Comment on the morphology of the red blood cells.
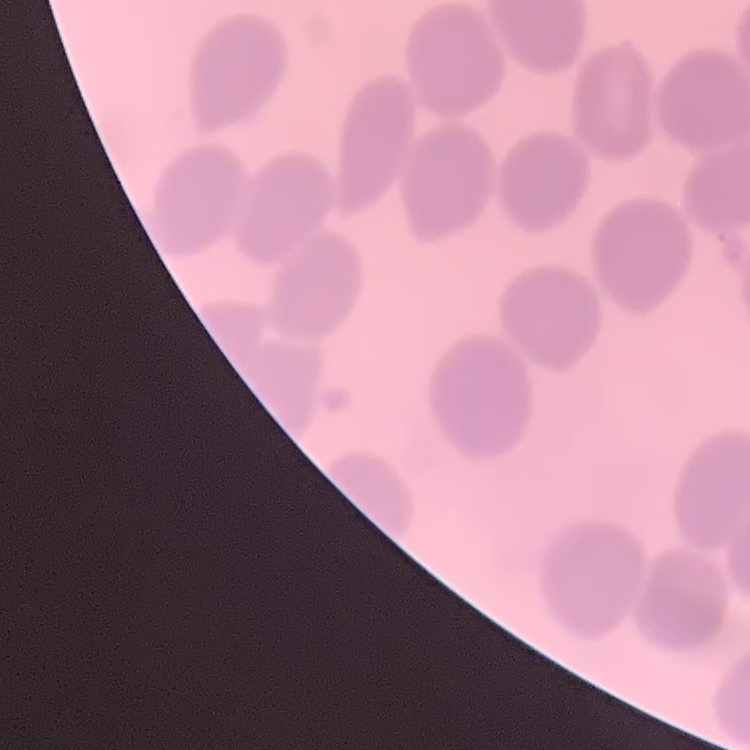

They show no rouleaux formation.

Thin peripheral smear. Square crop of a larger photomicrograph. Stained with either Field's or Giemsa.